Name the parasite shown.
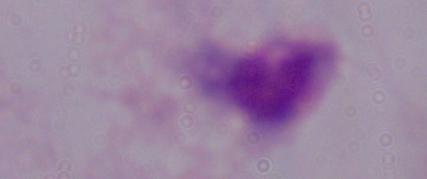
This is a trichomonad.

Photomicrograph. 1000x magnification.